Give the position of every Plasmodium parasite.
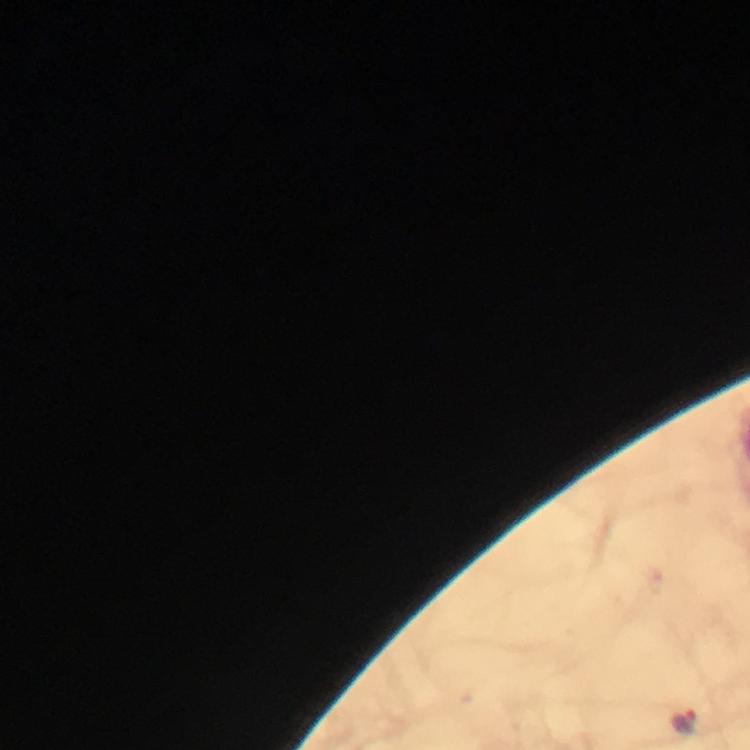
Approximate centers as {x, y} in pixels.
Plasmodium parasites: {683, 722}.

Summary:
  - Preparation: thick blood film
  - Immersion oil: used
  - Context: from a diagnostic examination for malaria
  - Cropped from: one field of view
  - Capture: smartphone photograph through a microscope
  - Stain: Giemsa
  - Image size: 750×750 pixels
  - Magnification: 100x